Identify the parasite.
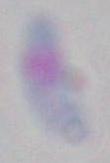
This is Toxoplasma gondii.

magnification: 1000x
modality: micrograph